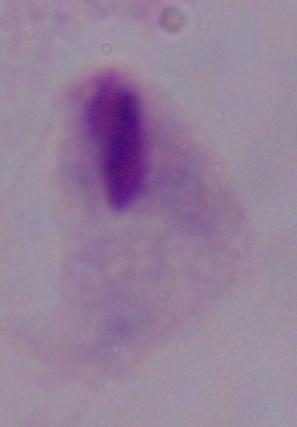

{
  "identification": "trichomonad",
  "modality": "photomicrograph",
  "magnification": "1000x"
}